State which parasite is depicted.
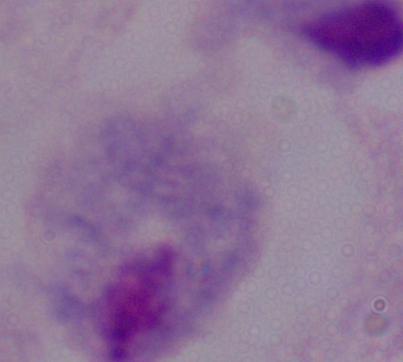
A trichomonad.

Summary:
  - Modality: micrograph
  - Magnification: 1000x